Assess this cell for malaria.
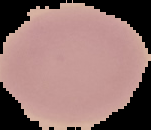
It is uninfected.

From a thin blood smear. Image is 151×130 pixels. Segmented cell region on a black background.